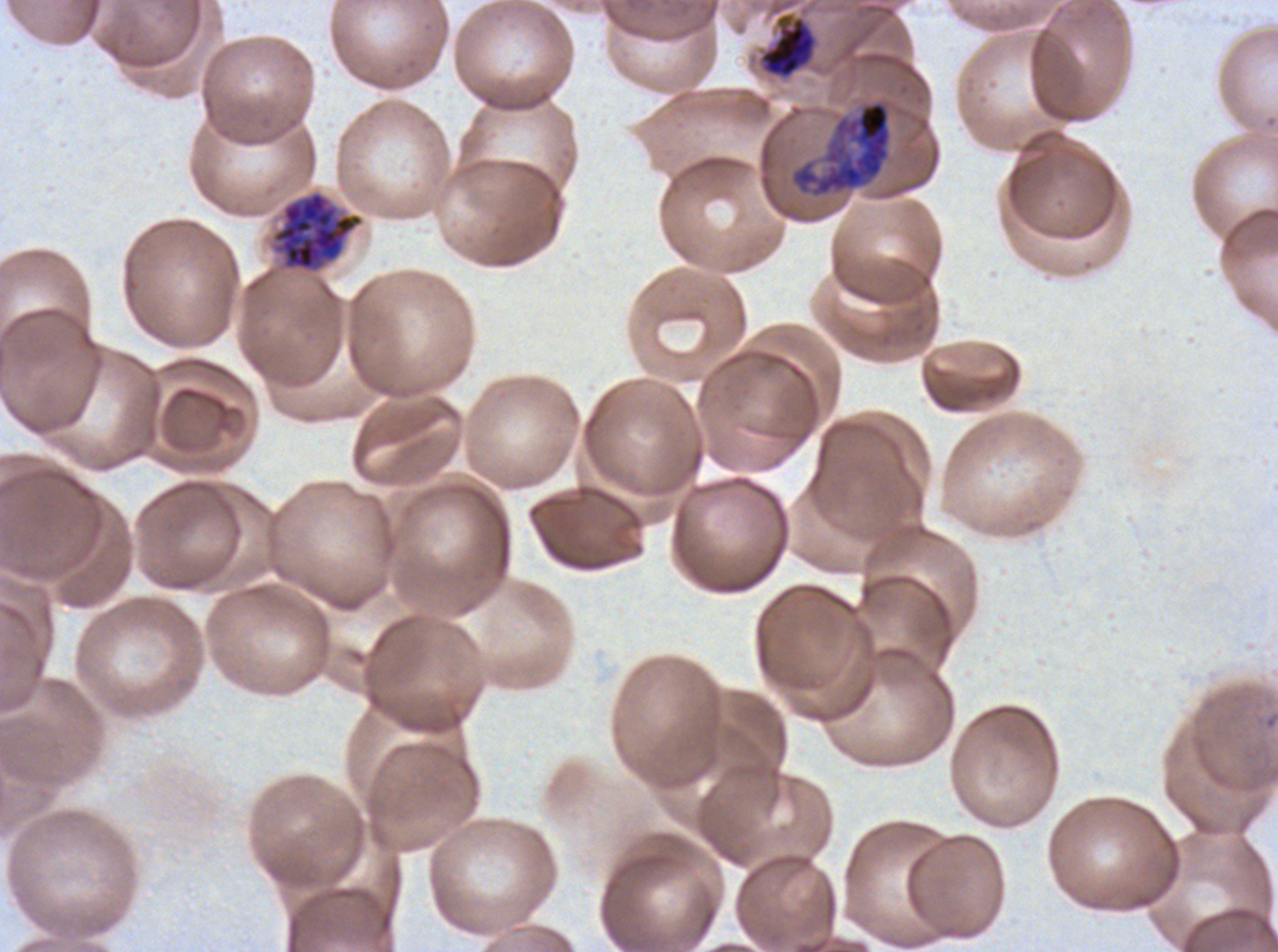

notation = approximate bounding boxes as [x1, y1, x2, y2] in pixels
late schizont locations = [790, 100, 892, 198], [271, 190, 364, 273]
late trophozoite locations = [758, 13, 817, 79]
field of view = one sub-image of a larger composite
stain = Giemsa
specimen = P. falciparum cultured ex vivo for 24 to 48 hours, from a patient in The Gambia
preparation = thin blood smear
image size = 1278×952 pixels
life-cycle stages observed = late trophozoite, late schizont